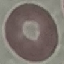

Result: negative for malaria parasites. Cell patch, automatically extracted from a larger field of view and resized to 64 × 64 pixels. Thin smear of blood. Giemsa stain. Acquired by smartphone through the microscope eyepiece.